Report the malaria status of this cell.
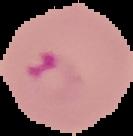
It is parasitized.

The area outside the segmented cell region is set to black. Image is 133×136 pixels. From a thin blood film.